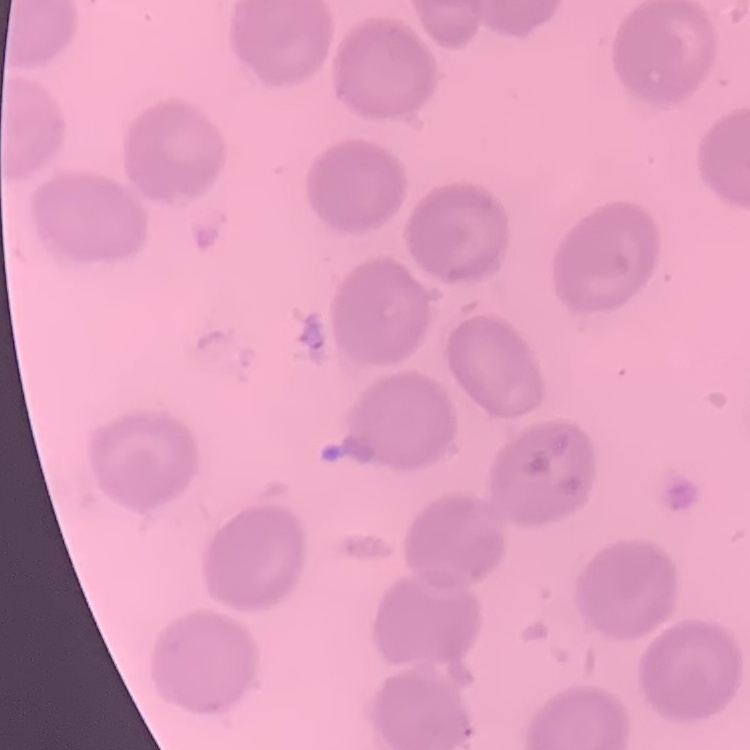

Summary:
  - Red blood cell morphology: no rouleaux formation
  - Image type: square crop of a larger photomicrograph
  - Stain: Field's or Giemsa
  - Preparation: thin blood film